Report the malaria status of this cell.
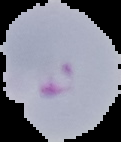
Parasitized.

Image is 121×142 pixels. From a thin blood film. Cell region segmented out of the field of view; the surrounding area is masked to black.